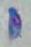

modality = photomicrograph
magnification = 1000x
identification = Toxoplasma gondii